Identify the cell.
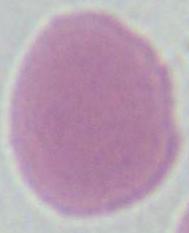
This is an erythrocyte.

Summary:
  - Modality: photomicrograph
  - Magnification: 1000x